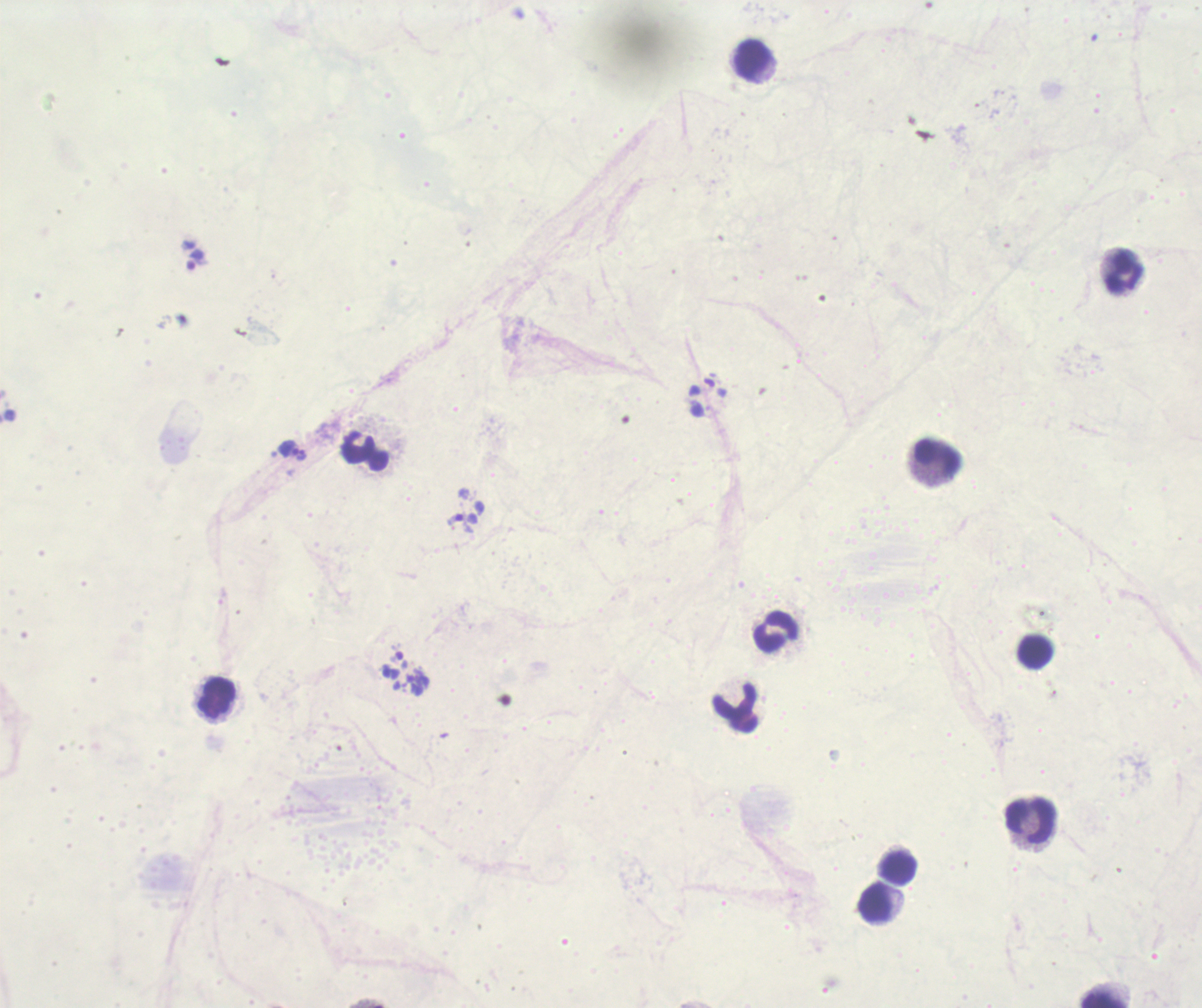
Approximate centers as (x, y) in pixels. Trophozoite locations: (194, 261), (291, 452). Leukocyte locations: (752, 61), (1121, 271), (364, 452), (935, 460), (774, 633), (1034, 651), (217, 700), (735, 705), (1028, 819), (897, 867), (876, 905), (1103, 1000). Thick blood smear. One field from this slide. Image is 1202×1008 pixels. Coloration quality: bad. Background quality: unsatisfactory. Previously used in a real diagnosis. Result: Plasmodium parasites detected. 100x magnification. Romanowsky-stained preparation.